Locate every malaria parasite.
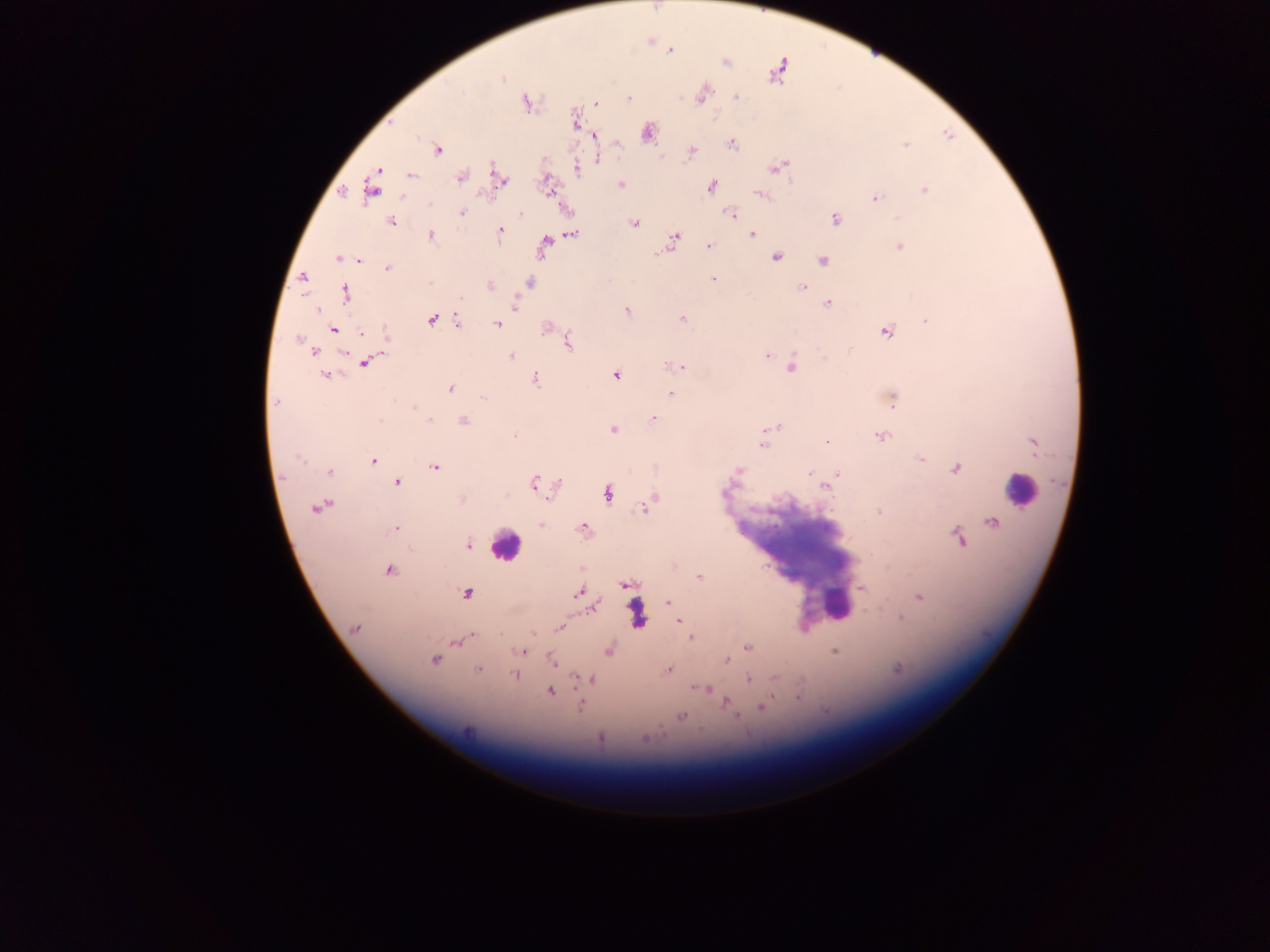
Approximate centers as {x, y} in pixels.
Malaria parasites: {670, 50}, {726, 63}, {777, 70}, {502, 78}, {702, 94}, {736, 97}, {628, 98}, {527, 103}, {596, 103}, {574, 120}, {648, 132}, {595, 136}, {732, 144}, {906, 144}, {438, 150}, {692, 151}, {599, 159}, {778, 167}, {577, 168}, {378, 170}, {411, 175}, {461, 176}, {500, 179}, {620, 184}, {548, 186}, {371, 187}, {711, 187}, {924, 190}, {760, 195}, {875, 198}, {462, 213}, {520, 214}, {732, 214}, {835, 219}, {392, 222}, {634, 223}, {500, 231}, {572, 234}, {752, 235}, {431, 236}, {675, 237}, {545, 241}, {709, 246}, {900, 247}, {657, 253}, {776, 257}, {337, 258}, {359, 260}, {823, 260}, {387, 269}, {303, 277}, {713, 279}, {529, 283}, {490, 285}, {802, 286}, {345, 294}, {516, 304}, {829, 304}, {318, 310}, {627, 310}, {682, 318}, {432, 319}, {926, 320}, {458, 322}, {497, 324}, {545, 327}, {334, 329}, {385, 332}, {886, 332}, {362, 333}, {297, 339}, {568, 343}, {850, 349}, {314, 351}, {767, 355}, {511, 356}, {825, 357}, {366, 362}, {682, 366}, {792, 367}, {325, 375}, {616, 375}, {536, 379}, {450, 389}, {670, 394}, {483, 397}, {891, 400}, {275, 402}, {654, 418}, {380, 420}, {430, 420}, {464, 421}, {772, 428}, {613, 430}, {513, 435}, {880, 436}, {827, 441}, {1034, 444}, {762, 445}, {300, 460}, {373, 460}, {922, 460}, {434, 467}, {956, 469}, {739, 470}, {329, 472}, {809, 473}, {838, 474}, {398, 483}, {534, 483}, {558, 484}, {826, 488}, {607, 494}, {462, 499}, {652, 501}, {646, 507}, {316, 508}, {878, 512}, {992, 523}, {541, 525}, {583, 527}, {396, 529}, {959, 538}, {468, 545}, {389, 571}, {699, 577}, {626, 585}, {862, 588}, {578, 593}, {466, 594}, {919, 596}, {669, 603}, {594, 607}, {902, 618}, {679, 620}, {560, 627}, {355, 628}, {534, 634}, {691, 637}, {470, 638}, {456, 642}, {748, 648}, {608, 651}, {835, 651}, {523, 652}, {727, 660}, {434, 661}, {551, 661}, {668, 669}, {899, 669}, {478, 670}, {515, 674}, {749, 679}, {591, 680}, {705, 689}, {549, 691}, {799, 697}, {727, 702}, {581, 706}, {762, 707}, {682, 716}, {736, 716}, {469, 731}, {600, 738}, {644, 738}.

Leukocyte locations: {1021, 489}, {505, 546}, {836, 605}, {637, 614}. Thick blood smear. Image is 1270×952 pixels. Sample from Ghana. One field of view. Mobile-phone photograph taken through the microscope.